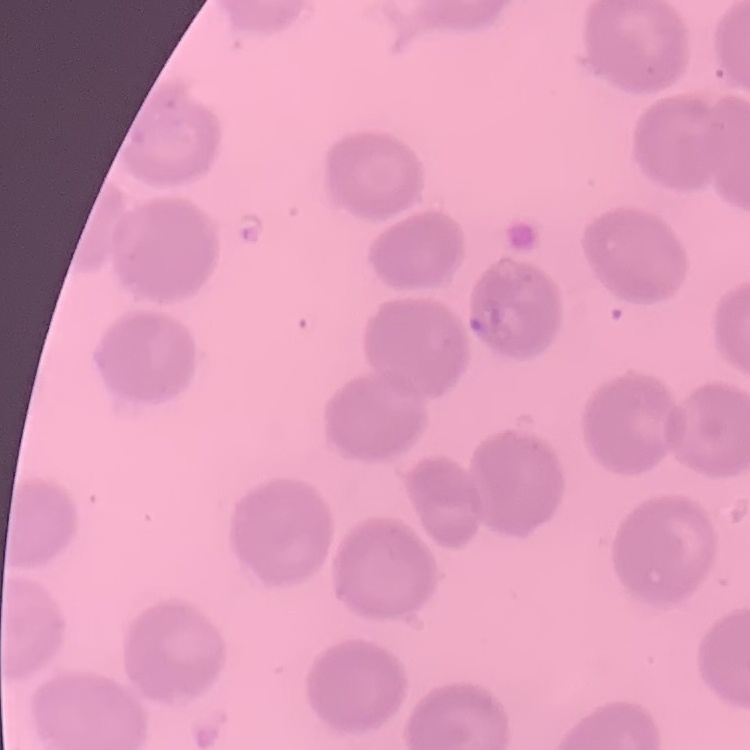

{
  "red_blood_cell_morphology": "no rouleaux formation",
  "stain": "Field's or Giemsa",
  "preparation": "thin blood smear",
  "image_type": "square crop of a larger photomicrograph"
}